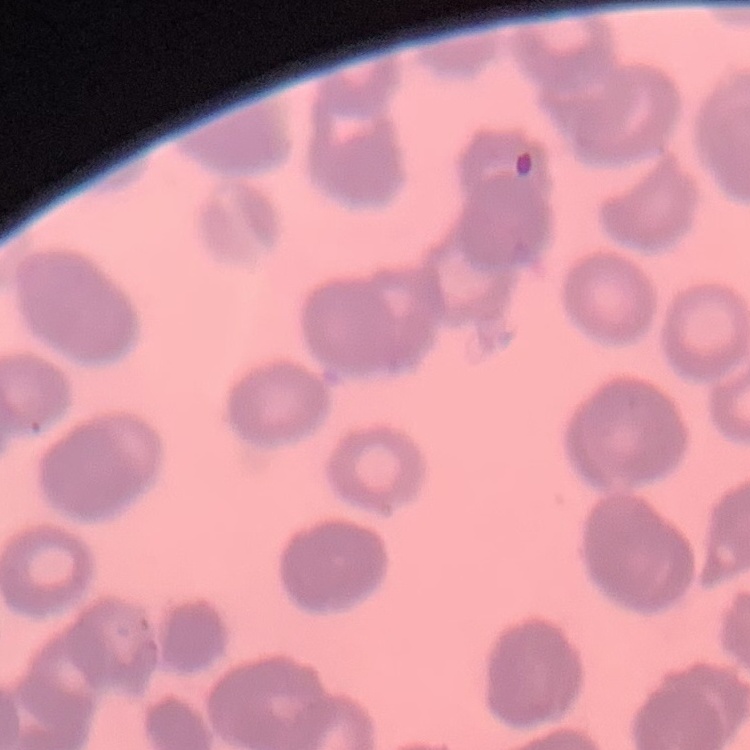

{
  "red_blood_cell_morphology": "rouleaux formation",
  "image_type": "square crop of a larger photomicrograph",
  "preparation": "thin peripheral smear",
  "stain": "Field's or Giemsa"
}